Locate every leukocyte (white blood cell).
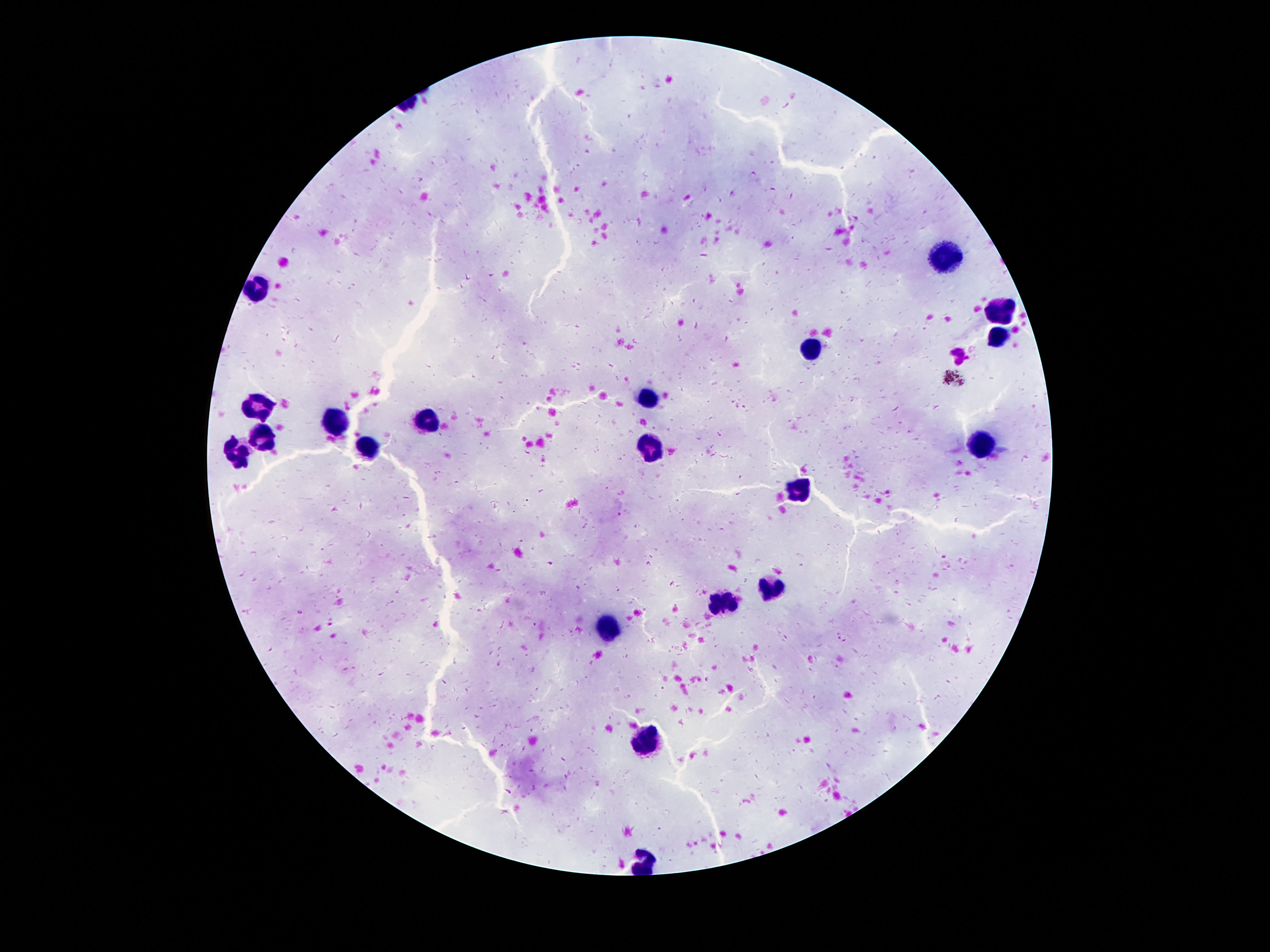

Approximate centers as (x, y) in pixels.
Leukocytes: (944, 256), (260, 288), (1002, 310), (996, 336), (812, 346), (646, 396), (260, 408), (426, 418), (338, 420), (262, 440), (980, 444), (368, 446), (650, 446), (232, 452), (800, 488), (772, 586), (726, 600), (602, 628), (648, 739).

capture: smartphone camera through the microscope eyepiece
image_size: 1270×952 pixels
patient_malaria_status: uninfected
magnification: 100x
stain: Giemsa
preparation: thick peripheral-blood smear
field_of_view: one from this slide